Locate every leukocyte (white blood cell).
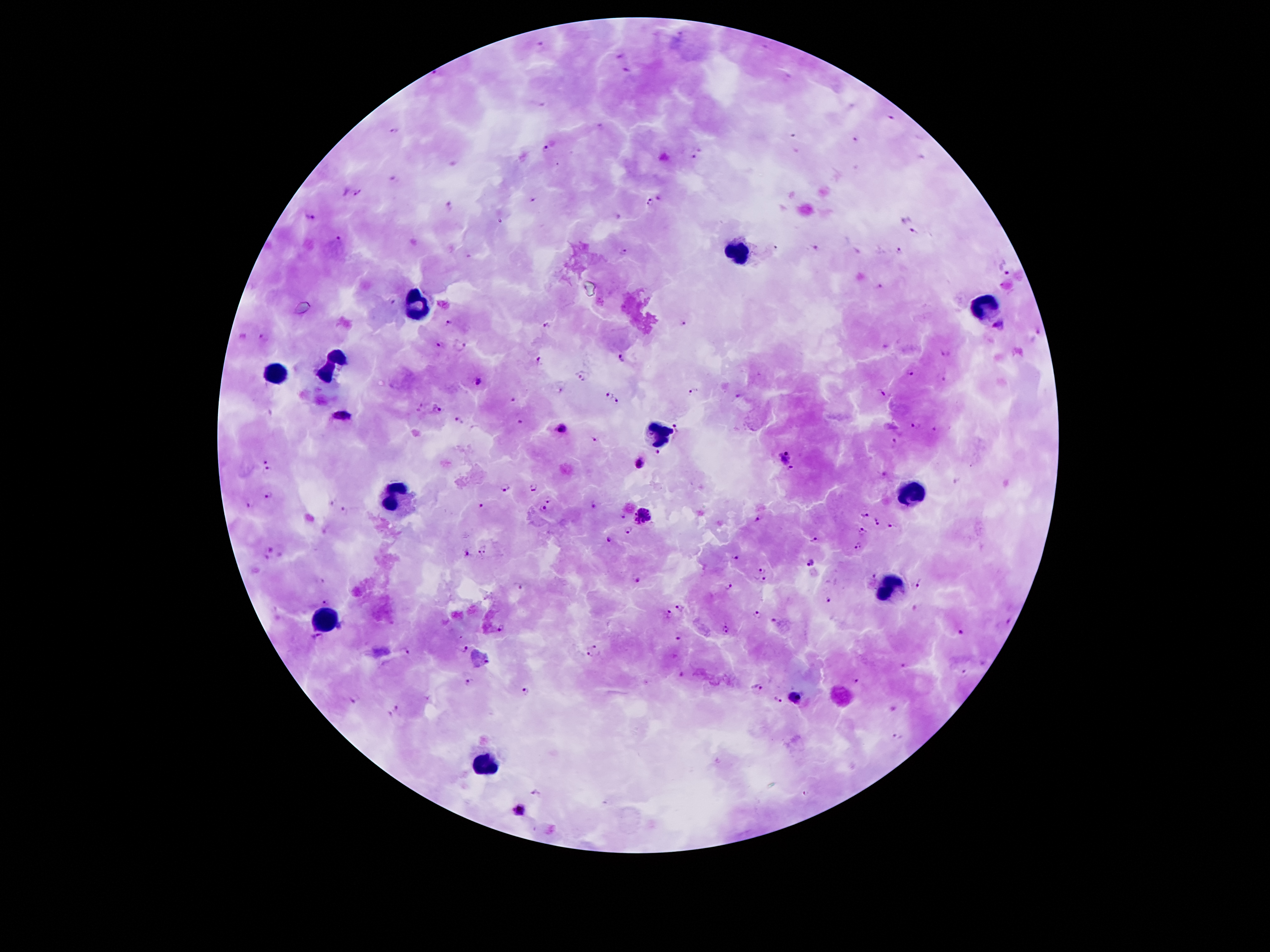
Approximate centers as (x, y) in pixels.
Leukocytes: (743, 251), (421, 305), (988, 305), (331, 367), (277, 375), (661, 430), (911, 494), (397, 500), (890, 586), (326, 619), (487, 761).

Plasmodium parasite locations: (542, 44), (628, 68), (790, 76), (542, 105), (892, 117), (395, 131), (855, 139), (547, 148), (703, 149), (694, 156), (358, 193), (658, 197), (534, 201), (650, 202), (450, 205), (307, 217), (914, 231), (338, 239), (815, 247), (624, 250), (899, 251), (1006, 271), (878, 287), (393, 302), (449, 323), (684, 323), (547, 324), (999, 326), (264, 336), (440, 343), (462, 346), (943, 353), (622, 357), (538, 359), (909, 373), (581, 377), (943, 379), (479, 380), (561, 389), (693, 392), (882, 392), (606, 394), (514, 397), (738, 398), (618, 401), (439, 408), (340, 415), (457, 419), (521, 421), (916, 425), (677, 427), (563, 428), (935, 430), (595, 440), (894, 441), (658, 453), (785, 458), (267, 461), (642, 463), (268, 472), (885, 475), (505, 488), (534, 488), (269, 497), (548, 500), (332, 503), (595, 504), (480, 505), (247, 506), (542, 508), (343, 510), (865, 513), (644, 515), (757, 516), (623, 517), (876, 521), (894, 526), (630, 530), (864, 531), (813, 539), (610, 541), (486, 547), (857, 547), (271, 549), (467, 553), (478, 555), (734, 559), (808, 563), (761, 570), (873, 576), (638, 579), (763, 579), (320, 581), (920, 582), (519, 584), (728, 587), (828, 599), (326, 602), (679, 608), (757, 613), (668, 614), (775, 618), (1009, 621), (500, 628), (725, 628), (961, 632), (678, 637), (316, 639), (594, 646), (465, 649), (404, 650), (589, 653), (487, 662), (902, 664), (964, 673), (681, 674), (857, 681), (468, 682), (757, 685), (527, 691), (796, 697), (354, 699), (778, 700), (395, 708), (389, 712), (896, 737), (537, 791), (519, 810). Patient malaria status: infected with Plasmodium falciparum. Giemsa stain. Smartphone photograph taken through the microscope eyepiece. Thick peripheral-blood smear. 100x magnification. Single field of view. Image is 1270×952 pixels.